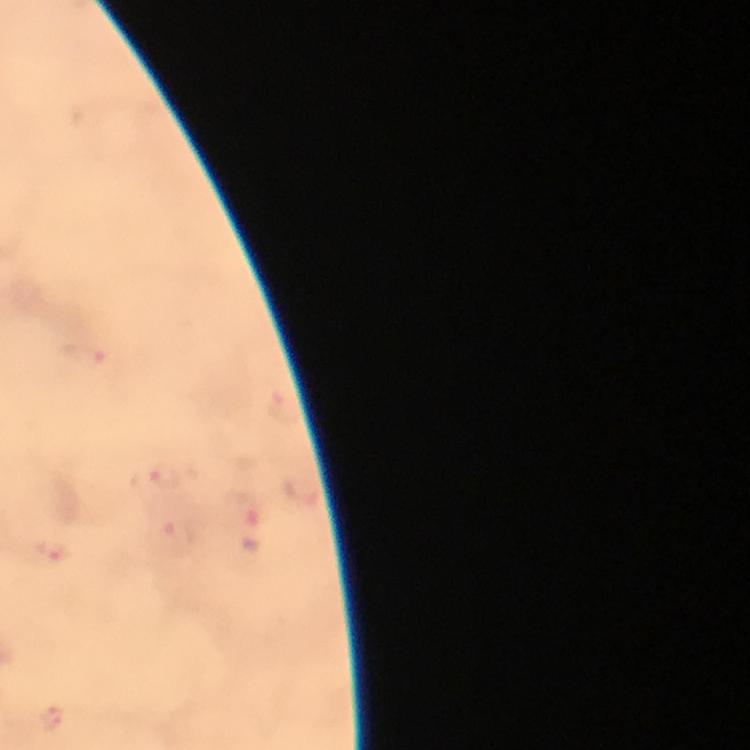

Approximate centers as (x, y) in pixels.
Summary:
  - Plasmodium parasite locations: (86, 353), (283, 408), (165, 478), (302, 491), (247, 509), (177, 537), (57, 552), (53, 720)
  - Context: from a malaria diagnostic workup
  - Image size: 750×750 pixels
  - Magnification: 100x
  - Preparation: thick blood smear
  - Stain: Giemsa
  - Cropped from: one field of view
  - Capture: smartphone mounted on the microscope
  - Immersion oil: applied